Locate every malaria parasite.
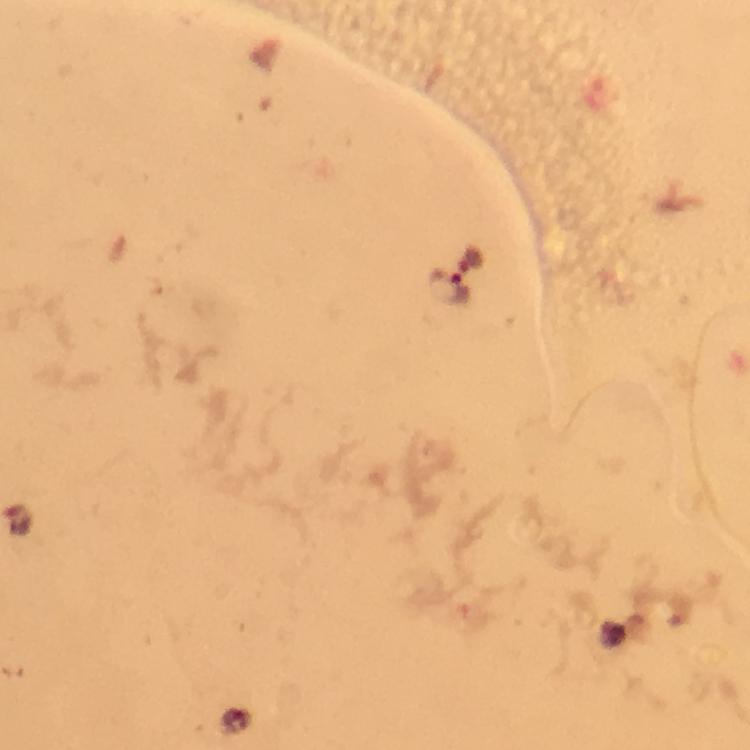
Approximate object centers, in pixels from the top-left corner.
Malaria parasites: (x=448, y=288).

Summary:
  - Magnification: 100x
  - Stain: Giemsa
  - Context: from a malaria diagnostic workup
  - Preparation: thick blood film
  - Cropped from: a single field of view
  - Immersion oil: used
  - Image size: 750×750 pixels
  - Capture: smartphone camera through the microscope